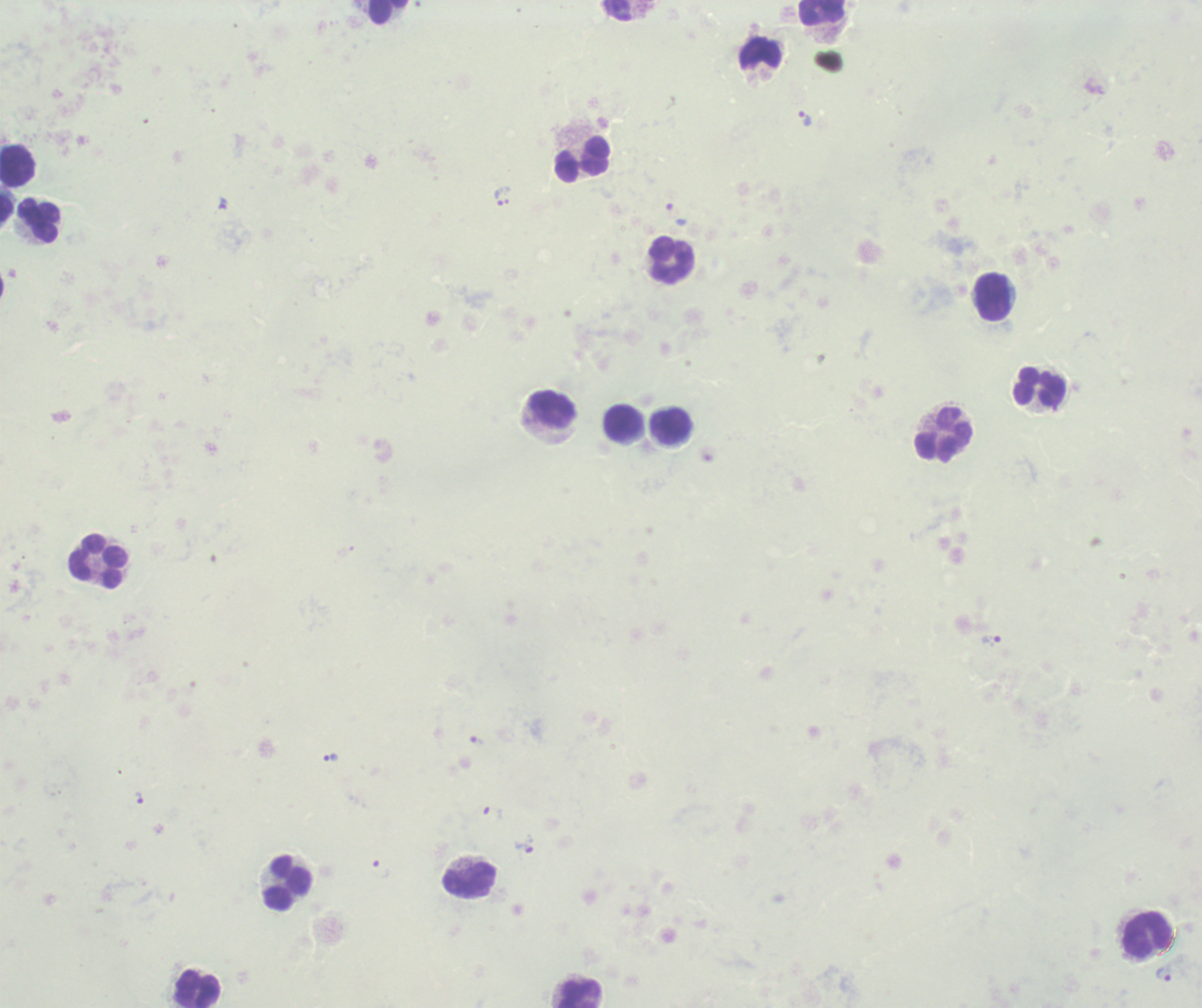 Approximate centers as (x, y) in pixels. Leukocyte locations: (617, 10), (388, 12), (822, 12), (762, 53), (582, 159), (17, 166), (6, 209), (38, 221), (672, 259), (994, 297), (1039, 387), (553, 409), (621, 422), (670, 426), (944, 433), (98, 561), (469, 880), (288, 883), (1148, 933), (198, 988), (579, 993). Trophozoite locations: (804, 119), (506, 196), (497, 198), (990, 640), (477, 740), (331, 758), (139, 797), (525, 844), (1163, 974). Result: positive for Plasmodium parasites. Single field of view. Thick blood smear. Background quality: unsatisfactory. Previously used in an actual diagnosis. 100x magnification. Image is 1202×1008 pixels. Romanowsky-stained preparation.